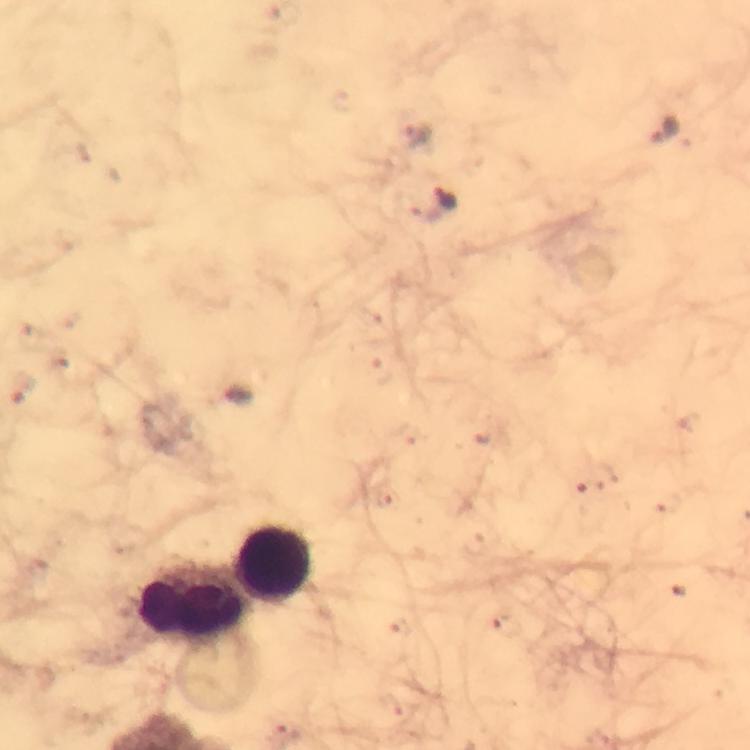

Approximate centers as [x, y] in pixels.
Summary:
  - Plasmodium parasite locations: [663, 129], [418, 133], [446, 198], [237, 397]
  - Leukocyte locations: [273, 565], [193, 603]
  - Stain: Giemsa
  - Immersion oil: used
  - Preparation: thick blood film
  - Image size: 750×750 pixels
  - Context: from a diagnostic examination for malaria
  - Magnification: 100x
  - Cropped from: one field of view
  - Capture: smartphone photograph through a microscope